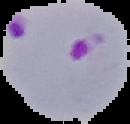 Image is 130×124 pixels. Result: malaria parasites detected. The area outside the segmented cell region is set to black. From a thin blood film.